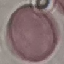

malaria_status: uninfected
stain: Giemsa
preparation: thin blood smear
image_type: automatically extracted cell patch, resized to 64 × 64 pixels
capture: smartphone camera at the microscope eyepiece